Outline each uninfected red blood cell.
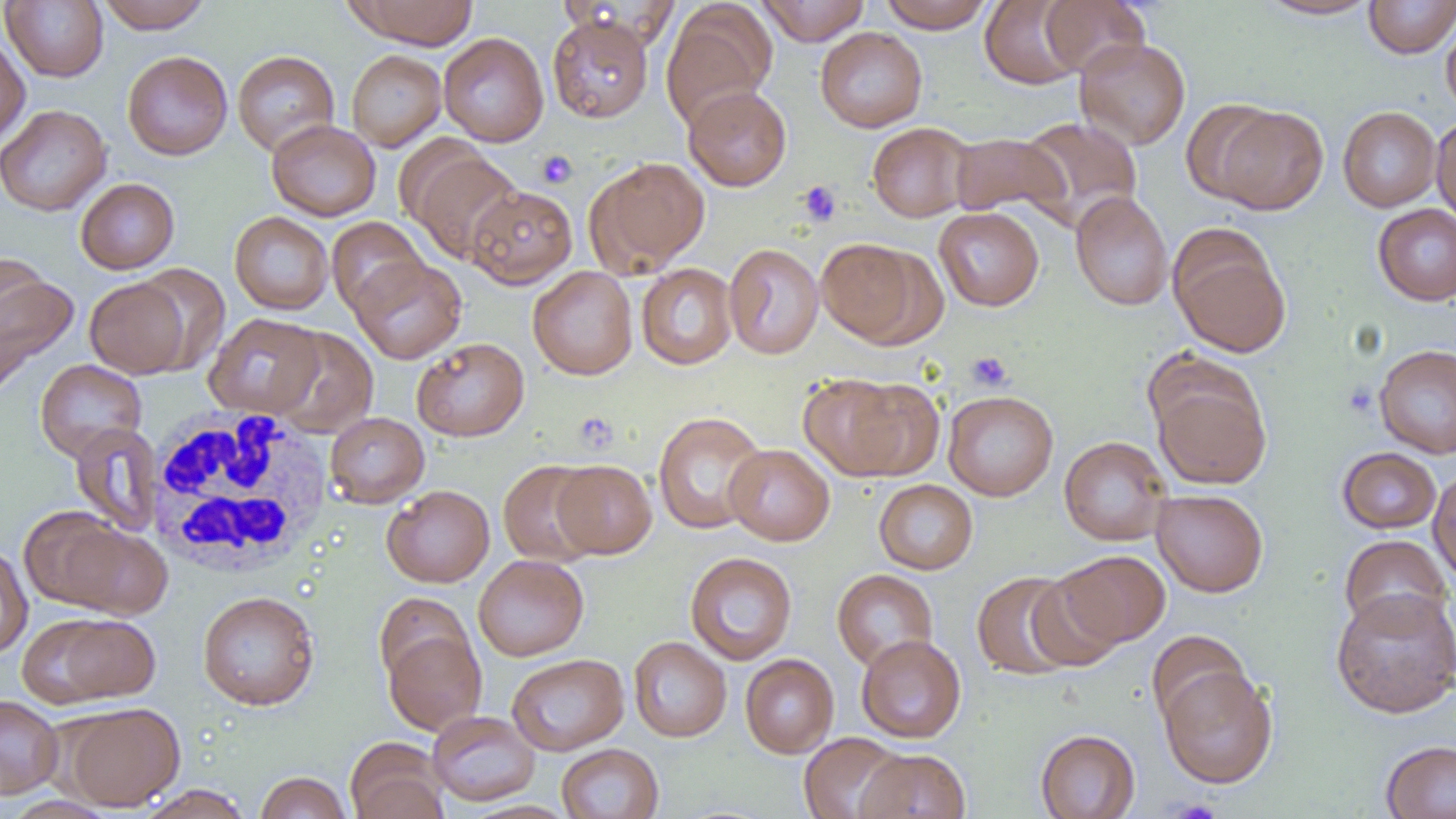

Approximate bounding boxes as (x1,y1)-(x2,y2) corner pairs in pixels.
Uninfected red blood cells: (96,0)-(212,33), (346,0)-(479,49), (756,0)-(870,45), (878,0)-(996,33), (980,0)-(1085,89), (1038,0)-(1150,77), (1256,0)-(1382,20), (1363,0)-(1456,59), (1,1)-(108,82), (661,3)-(777,130), (547,12)-(654,123), (1441,14)-(1456,119), (815,27)-(927,132), (438,32)-(549,147), (0,33)-(30,148), (1074,37)-(1191,149), (346,49)-(446,152), (122,50)-(233,160), (232,50)-(340,156), (683,85)-(792,191), (1179,98)-(1286,204), (0,104)-(111,216), (1211,104)-(1329,215), (1338,106)-(1442,212), (1431,115)-(1456,226), (1017,116)-(1143,230), (266,119)-(381,221), (867,122)-(974,223), (949,132)-(1071,219), (409,149)-(523,265), (587,157)-(710,275), (75,178)-(179,274), (467,185)-(577,288), (1070,191)-(1173,311), (1372,203)-(1456,306), (933,206)-(1044,311), (229,211)-(334,315), (327,216)-(428,316), (1169,229)-(1291,358), (815,237)-(934,346), (724,243)-(824,359), (0,252)-(53,346), (350,256)-(466,364), (636,263)-(738,370), (129,264)-(231,374), (0,266)-(78,385), (527,266)-(638,380), (85,276)-(193,378), (204,313)-(324,418), (270,327)-(378,438), (411,337)-(529,441), (1373,344)-(1456,459), (35,359)-(147,461), (1147,362)-(1273,491), (798,373)-(928,481), (943,390)-(1058,501), (652,411)-(769,535), (325,412)-(429,508), (71,423)-(163,537), (1059,436)-(1172,546), (725,444)-(834,545), (1337,447)-(1442,534), (498,460)-(603,567), (552,460)-(657,558), (1428,467)-(1456,585), (873,479)-(978,574), (382,485)-(494,587), (1151,489)-(1268,597), (45,518)-(173,620), (1339,534)-(1452,636), (0,544)-(33,658), (1058,550)-(1171,648), (685,551)-(798,665), (473,554)-(589,661), (832,569)-(939,672), (971,570)-(1081,680), (1026,571)-(1125,673), (1330,587)-(1456,718), (197,590)-(320,710), (374,592)-(475,688), (29,612)-(162,706), (382,627)-(487,735), (1145,630)-(1251,730), (856,634)-(966,743), (628,636)-(731,742), (506,653)-(629,756), (740,654)-(839,758), (1158,665)-(1278,788), (0,694)-(64,798), (60,702)-(185,811), (427,710)-(540,806), (1035,729)-(1140,818), (799,732)-(906,819), (345,738)-(449,819), (1381,740)-(1456,819), (556,743)-(663,819), (856,748)-(971,819), (254,771)-(351,819), (133,784)-(255,819), (3,797)-(118,818), (461,800)-(577,819).

Summary:
  - Platelet locations: (536,149)-(578,189), (797,180)-(842,226), (967,350)-(1013,391), (574,412)-(618,453), (1168,799)-(1222,819)
  - White blood cell locations: (144,407)-(334,578)
  - Slide-level diagnosis: no evidence of blood parasites
  - Modality: optical microscopy
  - Field of view: single
  - Image size: 1456×819 pixels
  - Preparation: thin blood film
  - Magnification: 1000x